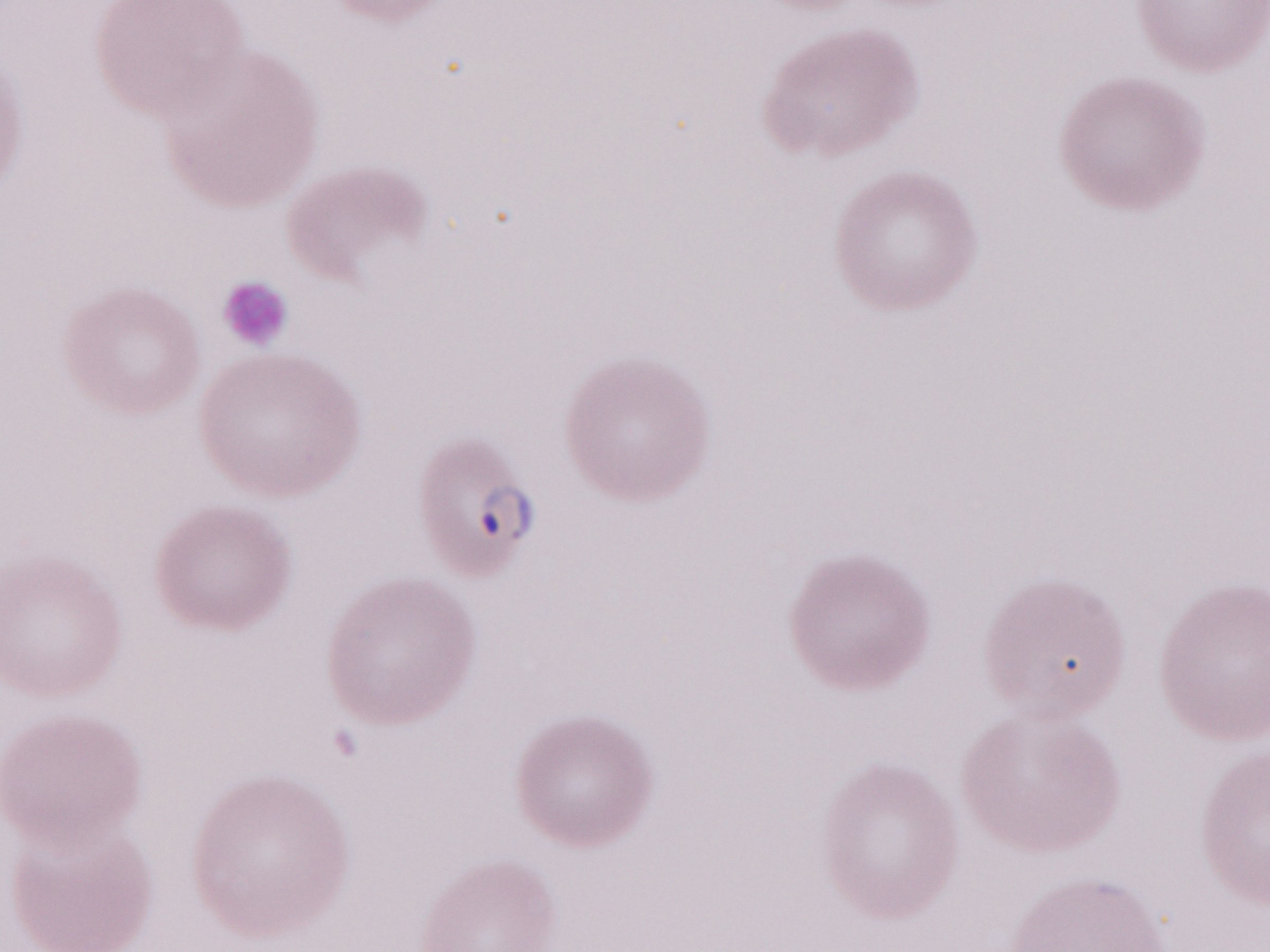
Thin blood smear. Single field of view. Malaria diagnosis (patient-level): positive. Olympus BX43 microscope and DP73 digital camera. Magnification: 1,000x. Image is 1270×952 pixels. May-Grünwald-Giemsa stain.